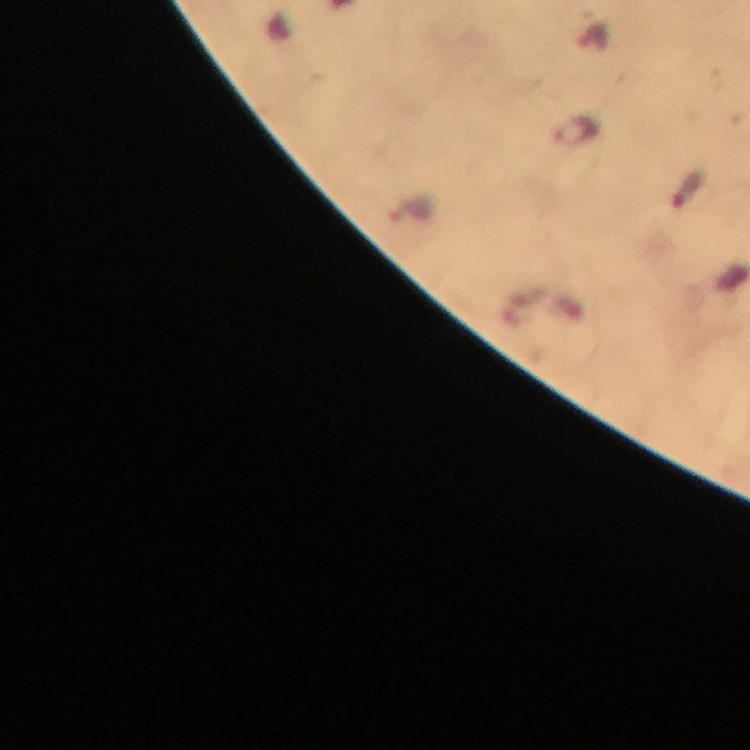
Approximate centers as [x, y] in pixels.
Summary:
  - Malaria parasite locations: [578, 132], [687, 190]
  - Preparation: thick blood film
  - Magnification: 100x
  - Stain: Giemsa
  - Image size: 750×750 pixels
  - Capture: smartphone mounted on the microscope
  - Immersion oil: applied
  - Context: from a diagnostic examination for malaria
  - Cropped from: one field of view